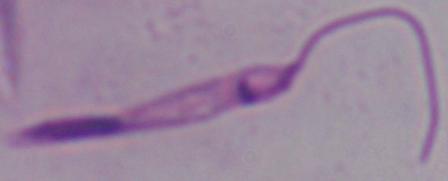 Micrograph. A Leishmania parasite is seen. Captured at 1000x magnification.